Assess this cell for malaria.
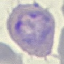
Parasitized.

{
  "preparation": "thin blood smear",
  "stain": "Giemsa",
  "capture": "smartphone through the microscope eyepiece",
  "image_type": "automatically extracted cell patch, resized to 64 × 64 pixels"
}